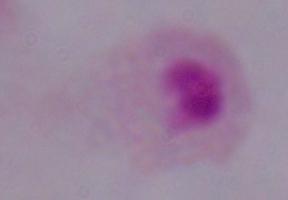
identification = trichomonad
modality = photomicrograph
magnification = 1000x